Report the malaria status of this cell.
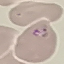

It is parasitized.

{
  "image_type": "cell patch, automatically extracted from a larger field of view and resized to 64 × 64 pixels",
  "capture": "smartphone through the microscope eyepiece",
  "stain": "Giemsa",
  "preparation": "thin blood smear"
}